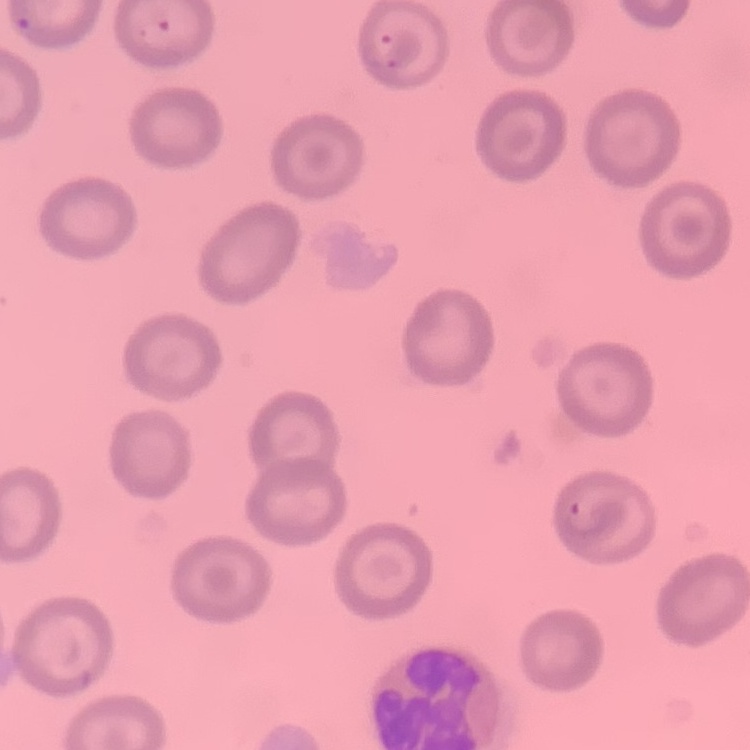
{
  "red_blood_cell_morphology": "no rouleaux formation",
  "preparation": "thin peripheral smear",
  "image_type": "one tile cut from a larger photomicrograph",
  "stain": "Field's or Giemsa"
}